Comment on the morphology of the red blood cells.
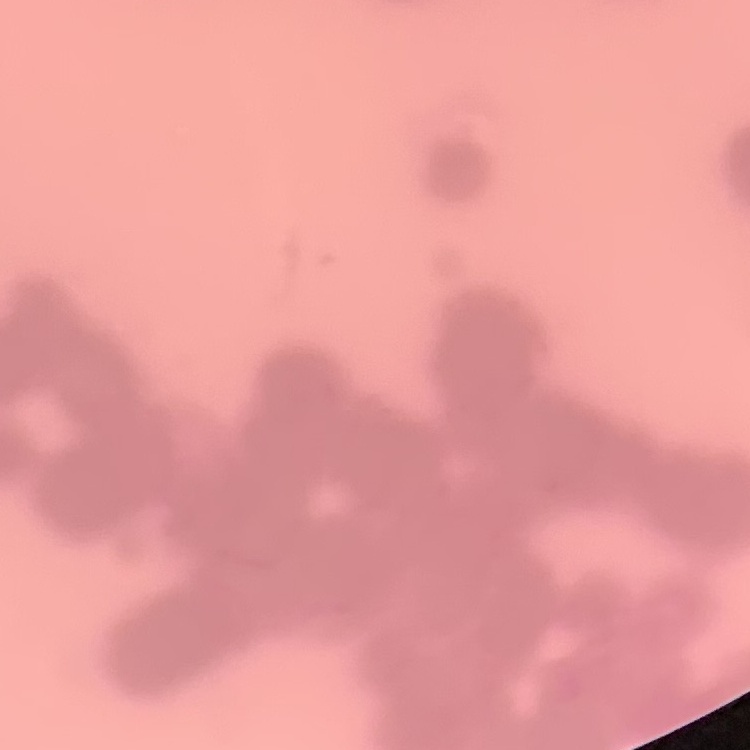

Rouleaux formation.

preparation = thin blood smear
stain = Field's or Giemsa
image type = square crop of a larger photomicrograph